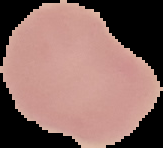
image type = segmented cell region with the area outside set to black
image size = 163×148 pixels
malaria status = uninfected
preparation = thin blood film